Give the extent of all Plasmodium ovale-infected red blood cells.
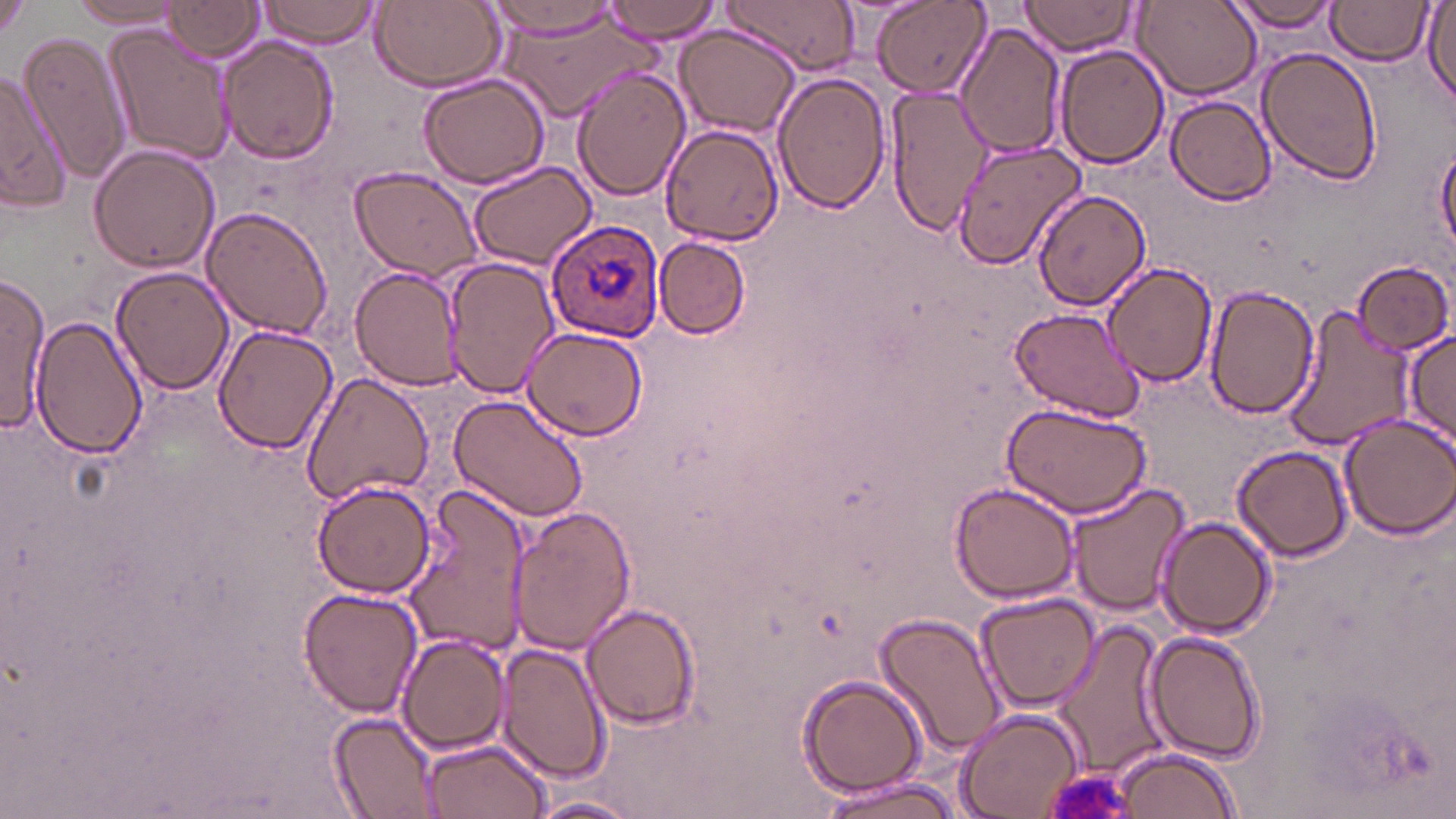
Approximate bounding boxes as [x1, y1, x2, y2] in pixels.
Plasmodium ovale-infected red blood cells: [547, 218, 664, 344].

slide_level_diagnosis: Plasmodium ovale
stain: May-Grünwald-Giemsa
image_size: 1456×819 pixels
modality: light microscopy
field_of_view: single
uninfected_red_blood_cell_locations: 'approximate bounding boxes as [x1, y1, x2, y2] in pixels: [257, 0, 385, 48], [598, 0, 723, 43], [724, 0, 863, 75], [875, 0, 989, 99], [1019, 0, 1137, 56], [1135, 0, 1260, 101], [1227, 0, 1344, 36], [66, 1, 186, 33], [160, 1, 265, 63], [373, 1, 507, 91], [483, 1, 628, 41], [1326, 1, 1431, 64], [1, 2, 31, 40], [1423, 2, 1456, 102], [498, 14, 659, 123], [955, 21, 1066, 163], [673, 23, 803, 138], [104, 26, 236, 165], [19, 28, 133, 186], [217, 36, 338, 164], [1256, 45, 1383, 183], [1057, 46, 1170, 168], [0, 66, 71, 211], [571, 66, 692, 204], [417, 69, 551, 188], [773, 71, 890, 212], [883, 86, 994, 236], [1166, 95, 1278, 205], [659, 123, 784, 246], [949, 139, 1088, 270], [88, 145, 220, 274], [1436, 146, 1456, 255], [469, 161, 596, 269], [349, 166, 485, 281], [1036, 191, 1152, 309], [200, 205, 332, 339], [655, 236, 752, 340], [443, 257, 559, 399], [1353, 259, 1454, 355], [1102, 262, 1218, 387], [110, 266, 234, 394], [349, 266, 465, 390], [0, 277, 49, 431], [1204, 285, 1319, 417], [1280, 306, 1415, 451], [1010, 307, 1146, 420], [32, 315, 145, 459], [213, 324, 337, 455], [519, 325, 647, 443], [1403, 328, 1456, 448], [301, 371, 435, 506], [448, 392, 590, 523], [999, 400, 1152, 516], [1335, 413, 1456, 538], [1232, 445, 1353, 562], [948, 480, 1083, 604], [1065, 480, 1188, 618], [312, 482, 436, 599], [401, 487, 531, 658], [507, 505, 637, 656], [1158, 516, 1276, 638], [296, 586, 422, 718], [976, 593, 1101, 712], [581, 601, 700, 731], [875, 609, 1008, 762], [1051, 617, 1172, 780], [1142, 630, 1266, 765], [396, 635, 509, 754], [498, 641, 608, 784], [796, 674, 928, 798], [953, 706, 1085, 819], [329, 710, 440, 817], [419, 738, 551, 819], [1108, 746, 1243, 818], [812, 773, 972, 819], [530, 795, 644, 818]'
magnification: 1000x
platelet_locations: 'approximate bounding boxes as [x1, y1, x2, y2] in pixels: [1042, 767, 1141, 819]'
preparation: thin blood film